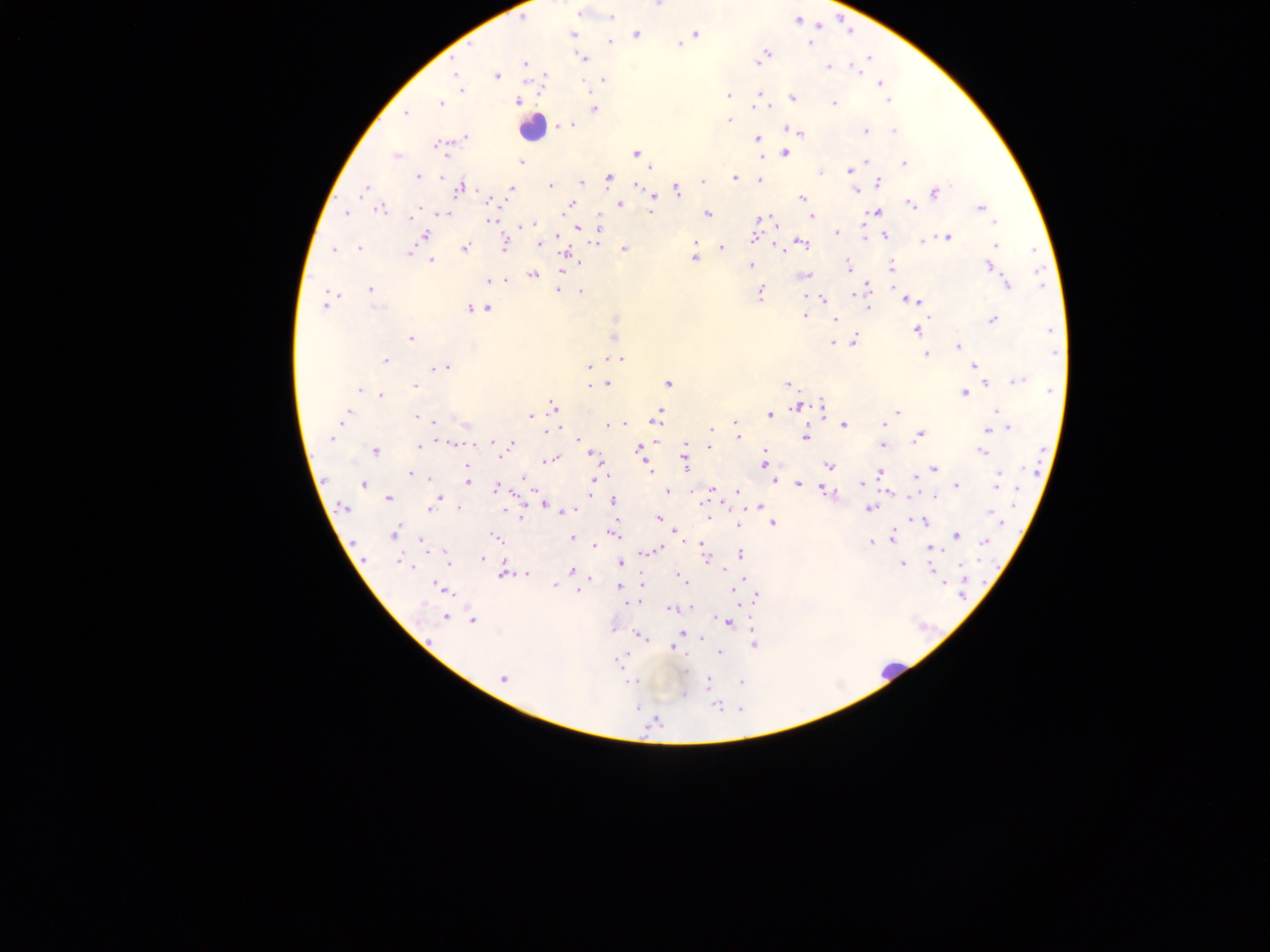

Approximate centers as (x, y) in pixels. Leukocyte locations: (531, 128), (890, 671). Plasmodium parasite locations: (578, 13), (611, 17), (797, 20), (696, 33), (573, 34), (637, 34), (611, 41), (811, 43), (679, 45), (763, 56), (583, 57), (758, 59), (525, 63), (829, 66), (856, 68), (455, 73), (496, 76), (603, 80), (880, 83), (461, 91), (759, 94), (728, 96), (793, 97), (888, 100), (517, 101), (440, 103), (833, 103), (594, 109), (406, 113), (729, 119), (569, 124), (895, 130), (796, 131), (866, 131), (466, 136), (757, 138), (438, 145), (785, 152), (636, 153), (396, 156), (865, 161), (521, 162), (904, 163), (651, 167), (850, 170), (821, 173), (418, 176), (443, 176), (609, 177), (736, 177), (702, 180), (760, 181), (581, 182), (880, 182), (551, 185), (638, 185), (461, 187), (511, 188), (364, 190), (678, 190), (854, 191), (935, 193), (653, 196), (802, 198), (491, 202), (619, 203), (912, 205), (570, 206), (420, 208), (981, 208), (381, 209), (651, 211), (345, 213), (444, 213), (875, 213), (707, 214), (412, 217), (812, 217), (761, 219), (489, 220), (530, 224), (524, 226), (599, 228), (578, 229), (837, 232), (426, 234), (885, 236), (948, 238), (756, 239), (596, 240), (923, 241), (800, 243), (505, 244), (539, 244), (996, 246), (722, 247), (358, 248), (465, 248), (624, 249), (334, 250), (409, 253), (566, 254), (694, 258), (431, 261), (848, 265), (751, 266), (989, 266), (563, 267), (892, 267), (533, 274), (804, 275), (504, 280), (489, 281), (1007, 284), (370, 289), (558, 291), (581, 292), (760, 293), (330, 294), (855, 294), (806, 296), (823, 299), (906, 299), (913, 301), (324, 306), (375, 307), (869, 307), (487, 308), (470, 309), (804, 315), (835, 319), (992, 320), (917, 331), (614, 336), (410, 338), (855, 340), (833, 342), (958, 347), (926, 354), (621, 358), (385, 360), (589, 366), (974, 366), (444, 368), (1018, 380), (668, 383), (607, 384), (788, 384), (986, 384), (590, 386), (414, 387), (358, 389), (1050, 390), (964, 393), (382, 394), (554, 406), (822, 406), (796, 407), (996, 411), (897, 412), (346, 415), (659, 415), (770, 415), (531, 416), (417, 417), (431, 421), (884, 422), (622, 424), (736, 424), (609, 426), (844, 426), (1009, 428), (711, 429), (988, 429), (547, 431), (919, 436), (805, 437), (332, 438), (738, 438), (578, 439), (490, 443), (511, 443), (686, 443), (452, 444), (709, 446), (883, 446), (419, 447), (640, 450), (374, 451), (981, 452), (593, 454), (501, 455), (549, 460), (684, 462), (765, 464), (829, 465), (466, 466), (649, 468), (934, 469), (880, 472), (410, 474), (601, 476), (915, 476), (998, 477), (430, 478), (524, 480), (773, 480), (467, 481), (799, 484), (863, 484), (364, 485), (592, 485), (956, 486), (496, 489), (712, 490), (590, 491), (668, 491), (826, 491), (737, 492), (439, 497), (935, 497), (388, 498), (613, 502), (434, 503), (543, 504), (759, 506), (344, 508), (869, 508), (459, 509), (430, 510), (570, 511), (991, 512), (520, 516), (658, 517), (920, 521), (773, 524), (737, 525), (394, 534), (615, 534), (677, 534), (956, 535), (493, 537), (894, 537), (573, 538), (422, 540), (871, 542), (985, 542), (593, 545), (662, 547), (656, 549), (933, 550), (650, 551), (741, 554), (706, 555), (483, 558), (400, 560), (448, 562), (620, 563), (903, 564), (932, 569), (572, 570), (725, 571), (503, 574), (526, 574), (682, 578), (942, 582), (642, 584), (553, 586), (618, 586), (442, 588), (577, 591), (734, 591), (756, 597), (634, 602), (629, 603), (671, 609), (445, 617), (473, 621), (728, 623), (681, 633), (639, 636), (701, 639), (754, 645), (673, 648), (720, 652), (617, 661), (503, 679), (635, 681), (741, 682), (708, 683), (684, 696), (636, 707), (717, 707), (655, 721). Thick blood film. Image is 1270×952 pixels. Sample from Ghana. Mobile-phone photograph taken through the microscope. One field of view.